Name the cell type shown.
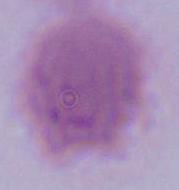
An erythrocyte.

modality = photomicrograph
magnification = 1000x